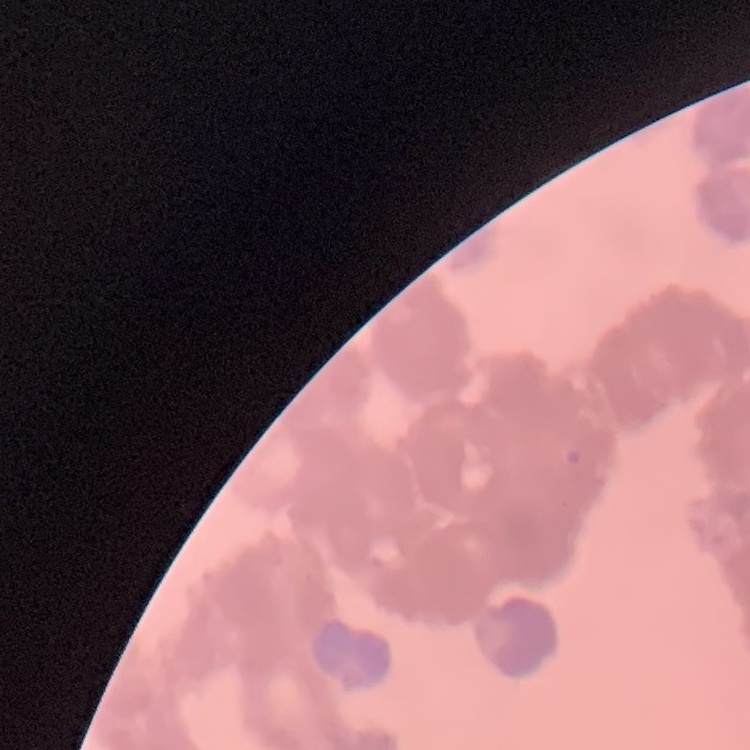

Summary:
  - Red blood cell morphology: rouleaux formation
  - Preparation: thin peripheral smear
  - Stain: Field's or Giemsa
  - Image type: square crop of a larger photomicrograph